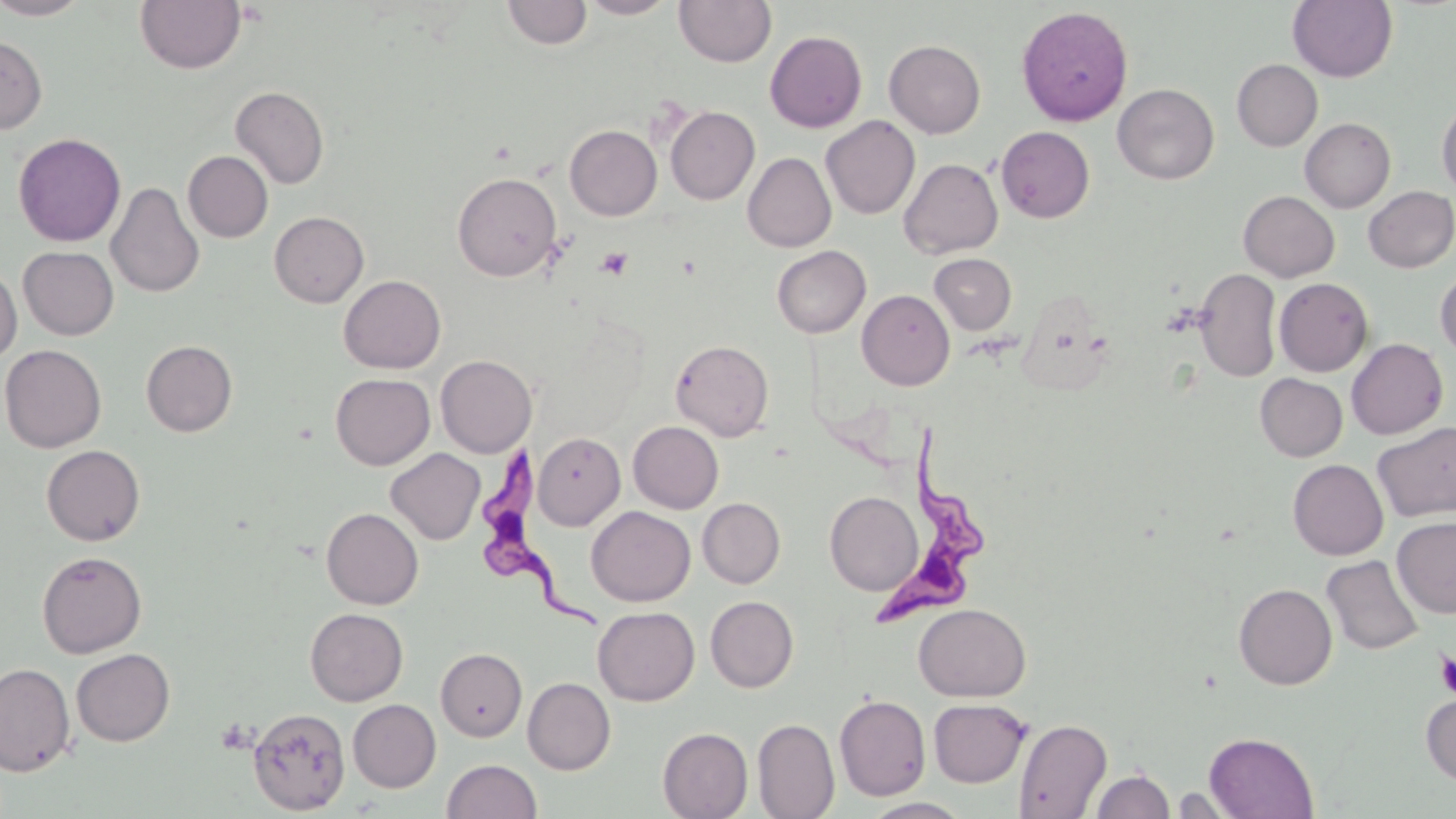
slide-level diagnosis = Trypanosoma brucei
image size = 1456×819 pixels
field of view = one of a larger specimen
magnification = 1000x
modality = light microscopy
platelet locations = approximate bounding boxes as named x1/y1/x2/y2 corners in pixels: (x1=595, y1=247, x2=634, y2=279), (x1=1434, y1=647, x2=1456, y2=701)
stain = May-Grünwald-Giemsa
preparation = thin blood film
uninfected red blood cell locations = approximate bounding boxes as named x1/y1/x2/y2 corners in pixels: (x1=0, y1=0, x2=92, y2=19), (x1=135, y1=0, x2=246, y2=74), (x1=503, y1=0, x2=592, y2=49), (x1=577, y1=0, x2=680, y2=19), (x1=673, y1=0, x2=776, y2=67), (x1=1288, y1=0, x2=1398, y2=83), (x1=1017, y1=6, x2=1133, y2=125), (x1=764, y1=30, x2=867, y2=132), (x1=0, y1=35, x2=46, y2=134), (x1=884, y1=39, x2=986, y2=138), (x1=1232, y1=59, x2=1322, y2=151), (x1=1113, y1=83, x2=1219, y2=184), (x1=230, y1=86, x2=329, y2=189), (x1=1437, y1=100, x2=1456, y2=197), (x1=665, y1=106, x2=759, y2=204), (x1=821, y1=115, x2=920, y2=219), (x1=1300, y1=118, x2=1395, y2=212), (x1=564, y1=125, x2=662, y2=220), (x1=996, y1=126, x2=1094, y2=223), (x1=13, y1=132, x2=126, y2=247), (x1=183, y1=151, x2=273, y2=242), (x1=742, y1=152, x2=836, y2=252), (x1=899, y1=158, x2=1003, y2=258), (x1=452, y1=172, x2=561, y2=281), (x1=106, y1=181, x2=204, y2=299), (x1=1363, y1=186, x2=1456, y2=272), (x1=1238, y1=190, x2=1340, y2=282), (x1=269, y1=211, x2=369, y2=307), (x1=772, y1=245, x2=870, y2=338), (x1=18, y1=246, x2=119, y2=339), (x1=929, y1=253, x2=1016, y2=334), (x1=0, y1=263, x2=22, y2=364), (x1=1194, y1=268, x2=1282, y2=382), (x1=1435, y1=269, x2=1456, y2=360), (x1=338, y1=274, x2=446, y2=374), (x1=1275, y1=277, x2=1373, y2=376), (x1=857, y1=289, x2=955, y2=390), (x1=1346, y1=338, x2=1448, y2=439), (x1=670, y1=339, x2=774, y2=441), (x1=141, y1=340, x2=237, y2=436), (x1=0, y1=344, x2=106, y2=453), (x1=435, y1=355, x2=536, y2=457), (x1=330, y1=373, x2=435, y2=470), (x1=1255, y1=373, x2=1348, y2=461), (x1=628, y1=421, x2=723, y2=513), (x1=1372, y1=421, x2=1456, y2=522), (x1=533, y1=432, x2=625, y2=529), (x1=41, y1=445, x2=145, y2=546), (x1=386, y1=448, x2=485, y2=545), (x1=1288, y1=459, x2=1388, y2=560), (x1=825, y1=491, x2=922, y2=595), (x1=697, y1=497, x2=785, y2=588), (x1=586, y1=506, x2=695, y2=606), (x1=321, y1=507, x2=423, y2=610), (x1=1392, y1=516, x2=1456, y2=618), (x1=36, y1=551, x2=147, y2=658), (x1=1321, y1=555, x2=1424, y2=655), (x1=1234, y1=583, x2=1337, y2=690), (x1=705, y1=596, x2=798, y2=692), (x1=913, y1=603, x2=1030, y2=701), (x1=593, y1=606, x2=699, y2=705), (x1=305, y1=608, x2=407, y2=706), (x1=71, y1=648, x2=175, y2=747), (x1=436, y1=648, x2=527, y2=741), (x1=0, y1=662, x2=76, y2=776), (x1=523, y1=677, x2=615, y2=775), (x1=1421, y1=692, x2=1456, y2=786), (x1=834, y1=694, x2=931, y2=801), (x1=929, y1=698, x2=1031, y2=787), (x1=348, y1=699, x2=440, y2=792), (x1=248, y1=707, x2=350, y2=815), (x1=752, y1=712, x2=931, y2=812), (x1=752, y1=718, x2=840, y2=819), (x1=1013, y1=718, x2=1112, y2=818), (x1=658, y1=727, x2=753, y2=818), (x1=1204, y1=732, x2=1318, y2=818), (x1=442, y1=759, x2=542, y2=819), (x1=1091, y1=769, x2=1174, y2=819), (x1=1171, y1=787, x2=1238, y2=817), (x1=862, y1=797, x2=973, y2=818)
Trypanosoma brucei locations = approximate bounding boxes as named x1/y1/x2/y2 corners in pixels: (x1=874, y1=422, x2=997, y2=629), (x1=475, y1=450, x2=611, y2=625)